Name the blood parasite species.
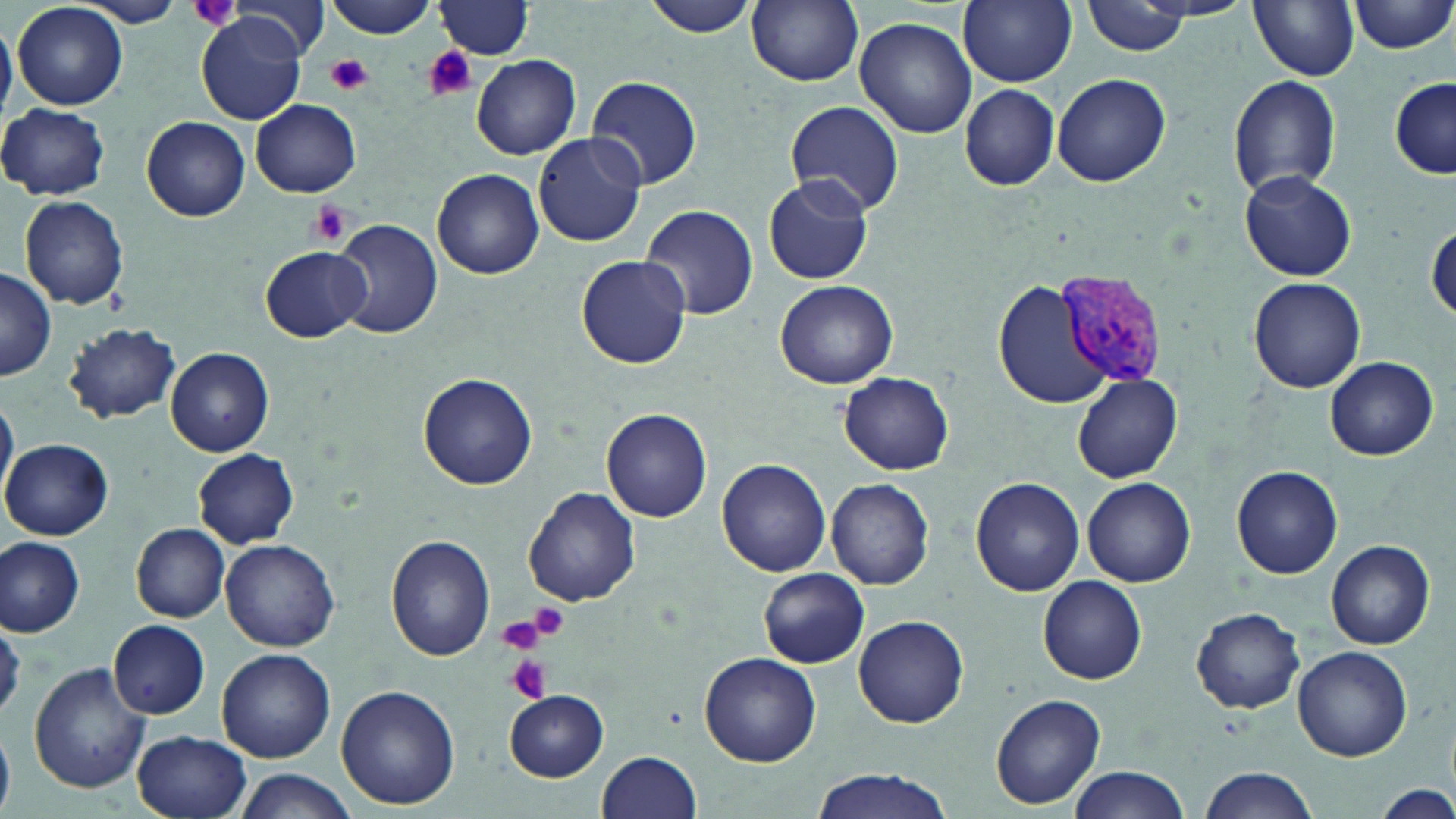
Plasmodium vivax.

Approximate bounding boxes as (x1, y1, x2, y2) in pixels. Platelet locations: (186, 0, 243, 32), (424, 46, 477, 102), (328, 55, 372, 96), (309, 201, 355, 246), (530, 603, 571, 640), (497, 614, 548, 654), (504, 653, 553, 704). Uninfected red blood cell locations: (81, 0, 184, 27), (324, 0, 439, 38), (642, 0, 764, 39), (958, 0, 1078, 87), (1082, 0, 1193, 55), (1349, 0, 1454, 55), (220, 1, 334, 63), (436, 1, 534, 57), (747, 1, 864, 87), (1249, 1, 1360, 80), (13, 2, 128, 111), (854, 16, 977, 138), (199, 17, 305, 124), (0, 18, 15, 123), (471, 54, 582, 159), (1052, 73, 1173, 186), (588, 75, 703, 189), (1226, 75, 1340, 200), (1389, 76, 1455, 178), (958, 84, 1060, 191), (249, 98, 362, 196), (783, 99, 905, 218), (0, 103, 110, 200), (136, 113, 361, 211), (141, 115, 249, 220), (531, 133, 647, 247), (431, 169, 543, 278), (1240, 170, 1356, 281), (763, 174, 874, 285), (20, 196, 130, 310), (639, 205, 758, 320), (331, 217, 443, 339), (1428, 224, 1456, 323), (260, 246, 370, 342), (575, 254, 691, 369), (0, 269, 57, 381), (1247, 277, 1366, 393), (774, 280, 898, 388), (994, 281, 1112, 409), (64, 324, 182, 424), (166, 347, 274, 456), (1324, 356, 1439, 461), (838, 372, 955, 473), (418, 373, 537, 490), (1073, 375, 1183, 483), (0, 392, 17, 507), (601, 408, 713, 523), (3, 438, 115, 541), (194, 449, 299, 547), (715, 459, 830, 577), (1232, 466, 1342, 578), (825, 476, 934, 591), (970, 477, 1084, 597), (1082, 477, 1196, 587), (524, 487, 642, 607), (133, 524, 230, 621), (387, 534, 496, 662), (0, 537, 85, 636), (220, 539, 341, 652), (1326, 540, 1435, 648), (759, 567, 870, 668), (1037, 576, 1147, 684), (1190, 606, 1306, 713), (852, 614, 970, 728), (1, 615, 25, 720), (110, 619, 210, 720), (1292, 645, 1412, 762), (217, 648, 335, 762), (699, 651, 821, 768), (30, 661, 151, 795), (335, 684, 459, 809), (503, 689, 609, 782), (990, 693, 1107, 809), (0, 728, 16, 817), (132, 730, 253, 819), (597, 750, 702, 819), (1066, 767, 1190, 819), (1194, 767, 1319, 819), (231, 769, 359, 819), (807, 770, 958, 819), (1375, 782, 1453, 818). Plasmodium vivax-infected red blood cell locations: (1054, 271, 1170, 393). Optical microscopy. Thin blood smear. One field of a larger specimen. May-Grünwald-Giemsa-stained preparation. Image is 1456×819 pixels. 1000x magnification.